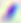
modality = photomicrograph
identification = Toxoplasma gondii
magnification = 400x